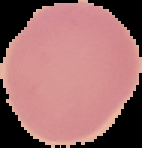

Malaria status: uninfected. Segmented cell region on a black background. Image is 142×148 pixels. From a thin blood smear.